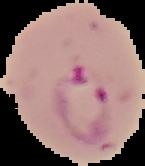
preparation = thin blood smear
image size = 145×166 pixels
image type = segmented cell region with the area outside set to black
result = Plasmodium parasites detected